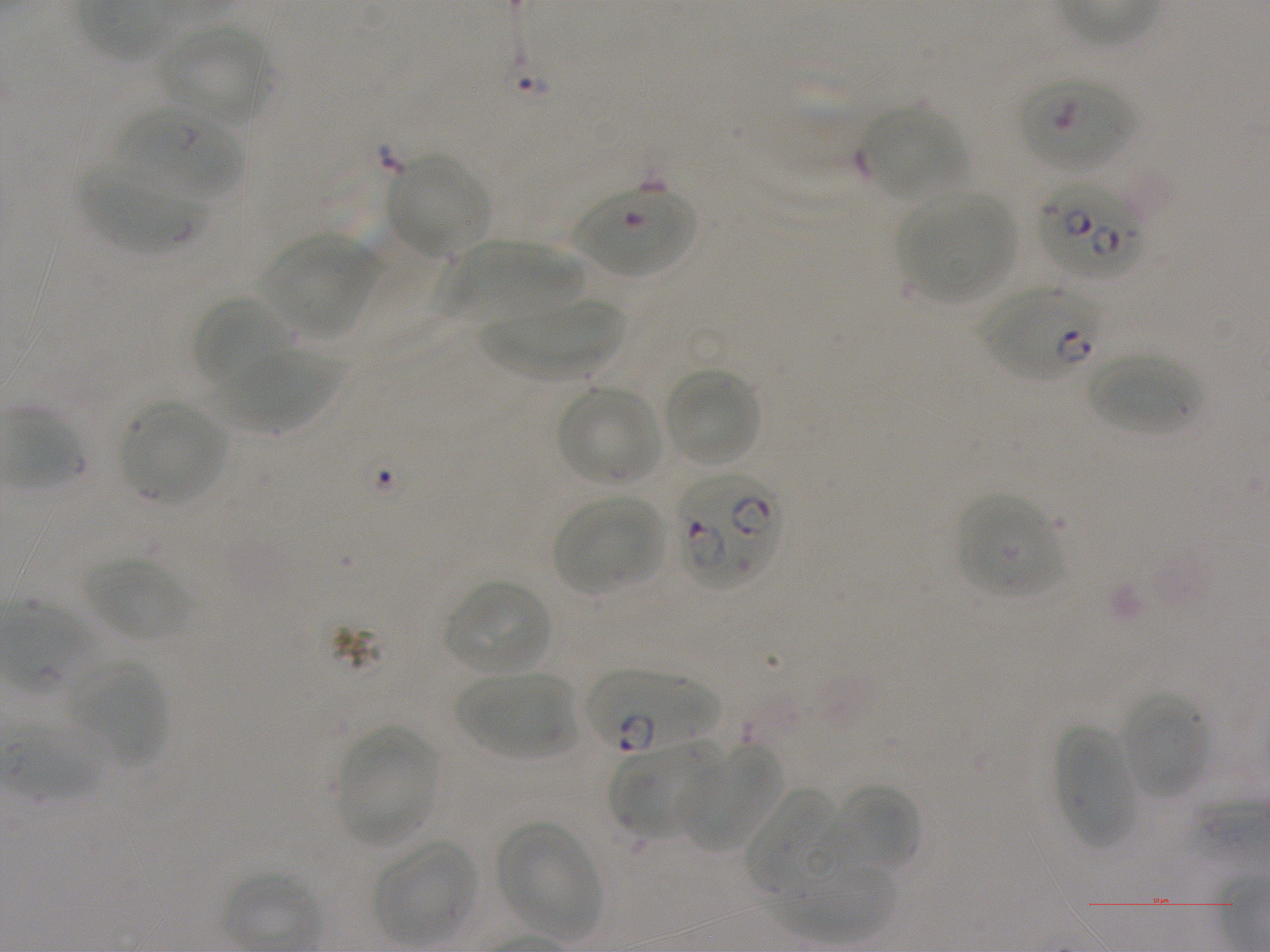
Approximate bounding boxes as [x1, y1, x2, y2] in pixels. Not every red blood cell is marked. A life-cycle stage — or a range of stages, where the recorded stages span more than one — follows each staged infected red blood cell.
Summary:
  - Locations of red blood cells of indeterminate infection status: [1017, 74, 1134, 173], [574, 184, 696, 277]
  - Locations of uninfected red blood cells: [158, 24, 273, 127], [863, 107, 965, 202], [387, 155, 490, 258], [79, 167, 201, 255], [899, 192, 1015, 303], [262, 235, 381, 338], [444, 239, 587, 320], [192, 298, 294, 388], [479, 300, 626, 382], [213, 351, 350, 431], [1087, 355, 1202, 435], [663, 368, 762, 467], [557, 386, 661, 486], [119, 400, 226, 505], [956, 493, 1065, 599], [553, 495, 664, 595], [85, 556, 190, 642], [443, 580, 552, 676], [70, 659, 167, 766], [456, 670, 576, 761], [1120, 692, 1208, 800], [1055, 722, 1140, 849], [7, 723, 103, 800], [336, 725, 440, 847], [610, 739, 722, 836], [679, 743, 784, 853], [827, 784, 920, 877], [746, 787, 843, 892], [496, 822, 601, 939], [373, 839, 476, 945], [775, 862, 899, 942]
  - Locations of infected red blood cells: [116, 106, 242, 202] ring; [1036, 179, 1145, 280]; [981, 284, 1103, 382] ring; [677, 474, 783, 589]; [2, 603, 99, 694] early ring; [583, 670, 720, 753]
  - Culture: static in-vitro Plasmodium falciparum strain NF54
  - Objective: 100x, oil immersion, numerical aperture 1.25
  - Stain: Giemsa
  - Donor blood group: A+
  - Field of view: single
  - Preparation: thin blood film
  - Image size: 1270×952 pixels